Report the malaria status of this cell.
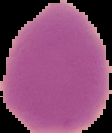
It is uninfected.

The area outside the segmented cell region is set to black. From a thin blood film. Image is 112×133 pixels.